Assess this cell for malaria.
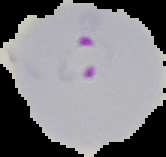

It is parasitized.

Segmented cell region on a black background. From a thin blood film. Image is 166×157 pixels.